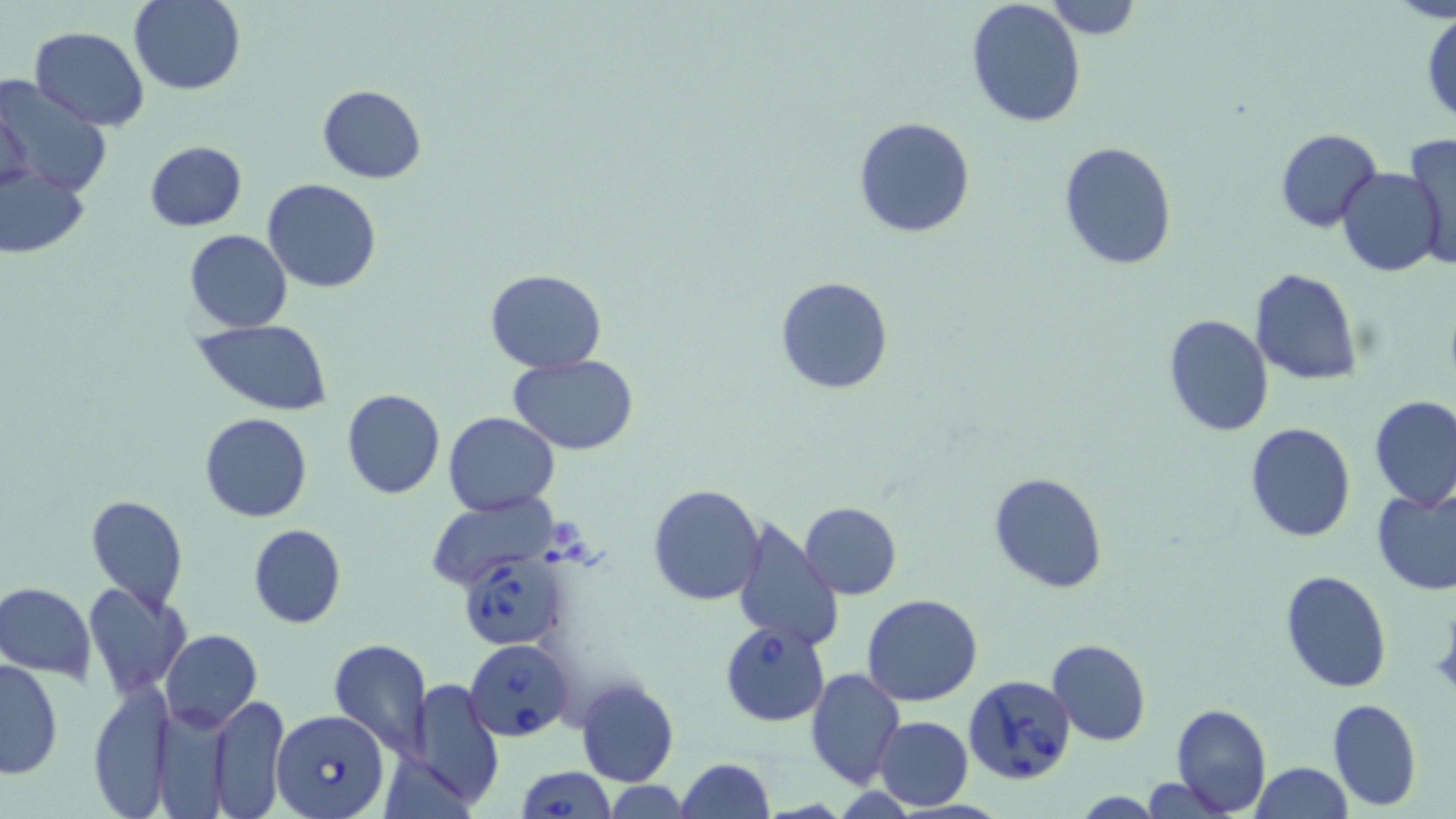

Approximate bounding boxes as [x1, y1, x2, y2] in pixels. Uninfected red blood cell locations: [1044, 0, 1142, 39], [130, 1, 246, 96], [967, 2, 1086, 130], [1422, 12, 1455, 126], [29, 26, 152, 128], [0, 73, 110, 198], [1, 82, 44, 202], [317, 85, 426, 184], [853, 117, 976, 238], [1274, 128, 1383, 233], [1405, 133, 1455, 266], [143, 141, 247, 230], [1059, 141, 1178, 269], [0, 163, 89, 261], [1336, 167, 1443, 277], [263, 178, 381, 294], [185, 229, 293, 333], [1250, 267, 1362, 385], [483, 268, 605, 373], [774, 276, 894, 395], [1163, 314, 1274, 436], [193, 320, 335, 414], [509, 355, 639, 453], [341, 389, 445, 500], [1369, 395, 1455, 510], [200, 412, 312, 523], [444, 412, 560, 515], [1243, 422, 1356, 543], [988, 471, 1109, 593], [648, 484, 765, 606], [1372, 485, 1456, 596], [427, 493, 557, 592], [85, 496, 188, 611], [798, 501, 902, 599], [731, 514, 844, 652], [248, 523, 345, 629], [1280, 569, 1392, 694], [0, 582, 97, 681], [81, 582, 190, 697], [862, 594, 985, 707], [160, 630, 262, 733], [328, 638, 434, 761], [1048, 638, 1152, 745], [1, 658, 64, 779], [805, 667, 905, 788], [575, 678, 678, 786], [406, 679, 503, 808], [86, 682, 177, 817], [211, 695, 291, 817], [1326, 697, 1421, 812], [1170, 704, 1271, 815], [874, 715, 973, 812], [675, 758, 775, 819], [1249, 762, 1351, 819], [603, 780, 693, 818]. Babesia divergens-infected red blood cell locations: [455, 551, 571, 651], [720, 622, 831, 728], [466, 639, 574, 740], [963, 674, 1075, 786], [270, 708, 389, 819], [516, 766, 613, 818]. Slide-level diagnosis: Babesia divergens. Light microscopy. Single field of view. 1000x magnification. Thin blood film. Image is 1456×819 pixels. May-Grünwald-Giemsa stain.